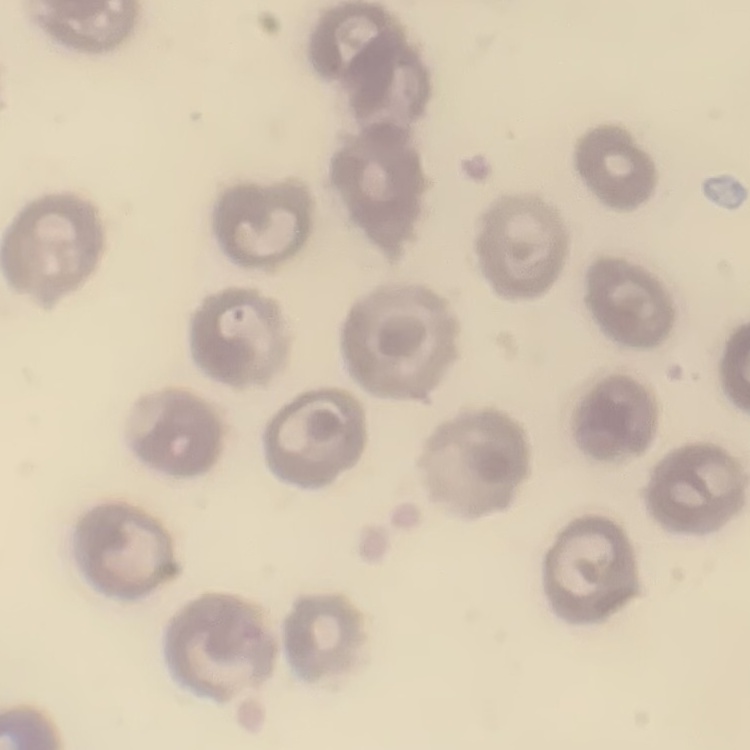

erythrocyte morphology = no rouleaux formation
preparation = thin blood film
image type = square crop of a larger photomicrograph
stain = Field's or Giemsa